Give the extent of all Plasmodium falciparum-infected red blood cells.
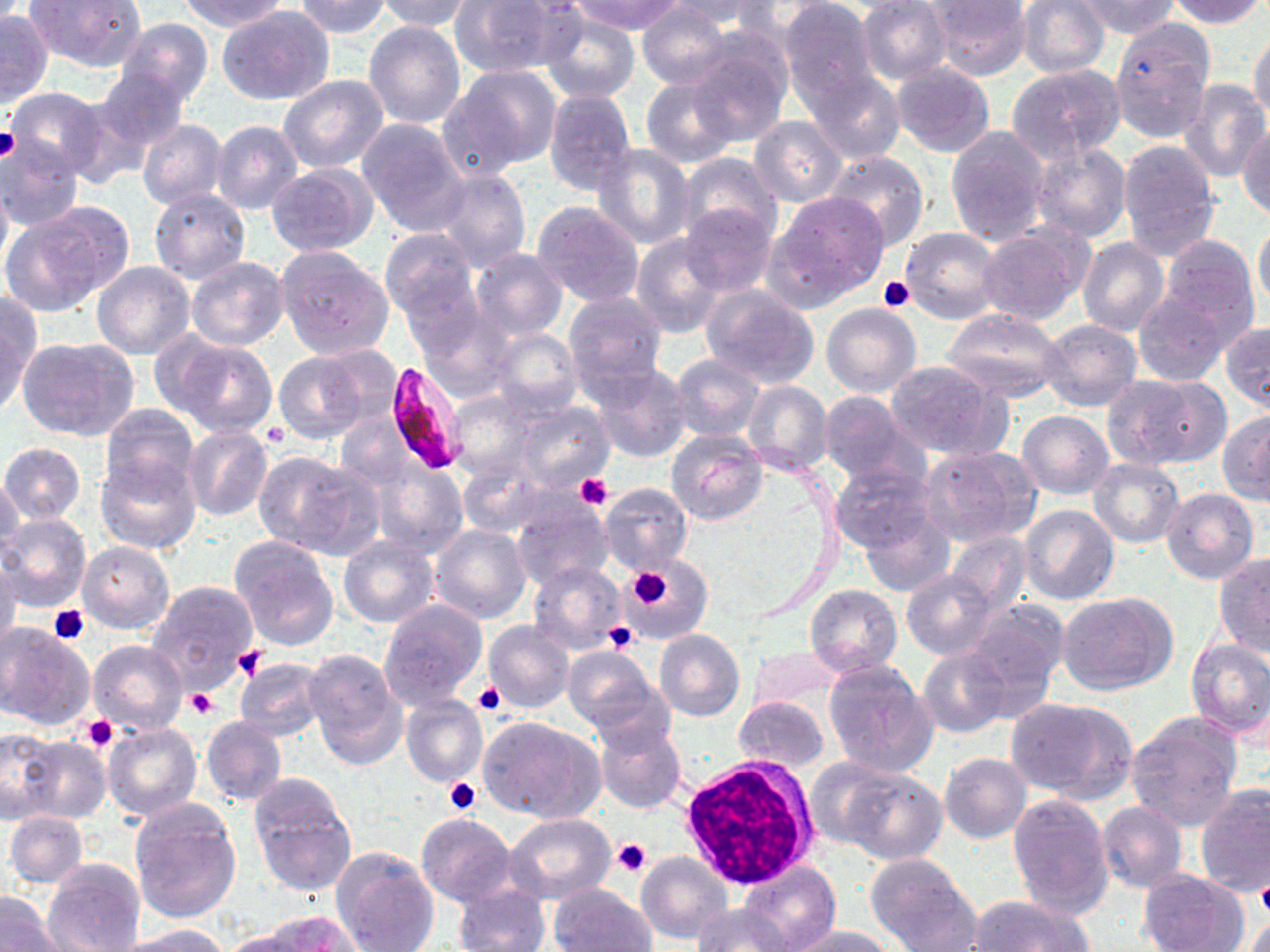

Approximate bounding boxes as [x1, y1, x2, y2] in pixels.
Plasmodium falciparum-infected red blood cells: [383, 361, 466, 475].

Summary:
  - White blood cell locations: [677, 756, 819, 887]
  - Platelet locations: [0, 128, 20, 163], [878, 276, 915, 313], [576, 474, 611, 510], [625, 566, 674, 609], [48, 604, 89, 645], [604, 621, 640, 654], [233, 645, 266, 679], [474, 681, 504, 715], [186, 689, 219, 719], [82, 714, 119, 753], [444, 777, 482, 815], [612, 838, 651, 877], [1255, 881, 1270, 917]
  - Uninfected red blood cell locations: [28, 0, 147, 72], [173, 0, 291, 32], [295, 0, 391, 38], [375, 0, 476, 33], [452, 0, 574, 81], [573, 0, 684, 36], [667, 0, 779, 30], [857, 0, 953, 86], [1073, 0, 1182, 39], [1163, 0, 1266, 27], [779, 1, 880, 107], [925, 1, 1031, 79], [1018, 1, 1111, 79], [636, 3, 730, 90], [217, 5, 334, 106], [538, 9, 640, 104], [0, 10, 52, 106], [115, 19, 215, 106], [363, 21, 466, 129], [1110, 24, 1215, 141], [1249, 26, 1270, 125], [683, 32, 792, 146], [891, 62, 995, 157], [1007, 63, 1125, 161], [444, 64, 563, 174], [94, 67, 189, 153], [804, 70, 905, 165], [279, 74, 389, 171], [640, 75, 741, 167], [1179, 79, 1269, 182], [5, 87, 109, 178], [1134, 87, 1258, 231], [543, 90, 636, 195], [748, 116, 848, 207], [211, 119, 304, 215], [357, 119, 470, 233], [136, 120, 228, 211], [1238, 124, 1270, 220], [944, 125, 1050, 244], [0, 138, 87, 232], [1116, 139, 1220, 256], [1029, 142, 1131, 242], [593, 144, 694, 249], [823, 150, 928, 249], [676, 153, 782, 247], [267, 162, 379, 258], [434, 166, 531, 271], [0, 174, 12, 285], [148, 186, 251, 282], [769, 192, 889, 305], [532, 201, 645, 306], [677, 201, 780, 298], [8, 203, 131, 312], [1254, 218, 1270, 315], [978, 225, 1090, 324], [900, 227, 1003, 324], [381, 228, 479, 322], [631, 233, 729, 337], [1156, 236, 1261, 341], [1077, 238, 1169, 337], [276, 247, 395, 358], [471, 247, 567, 338], [187, 256, 289, 350], [92, 262, 196, 359], [701, 285, 820, 388], [1131, 291, 1231, 384], [561, 292, 667, 391], [1, 294, 36, 412], [416, 299, 514, 397], [821, 303, 920, 396], [943, 306, 1065, 401], [1037, 319, 1141, 412], [1221, 322, 1269, 412], [488, 328, 582, 417], [19, 336, 139, 442], [168, 337, 279, 438], [275, 353, 372, 443], [672, 354, 763, 441], [884, 361, 1007, 459], [590, 364, 693, 463], [1107, 374, 1224, 469], [741, 381, 833, 477], [449, 390, 540, 479], [818, 391, 922, 485], [514, 401, 615, 493], [99, 403, 199, 500], [1018, 410, 1114, 499], [1218, 411, 1270, 506], [183, 426, 274, 521], [666, 429, 766, 524], [1, 442, 86, 524], [918, 444, 1040, 549], [252, 450, 376, 556], [96, 454, 201, 556], [458, 455, 549, 536], [369, 458, 467, 557], [1089, 458, 1184, 546], [830, 463, 936, 554], [1, 476, 25, 567], [600, 482, 692, 575], [1162, 488, 1259, 584], [510, 493, 613, 592], [1020, 504, 1119, 605], [859, 507, 956, 598], [0, 512, 91, 613], [429, 525, 531, 625], [946, 532, 1030, 614], [338, 535, 437, 627], [228, 536, 340, 650], [77, 541, 175, 634], [1214, 554, 1270, 653], [624, 557, 710, 641], [0, 558, 21, 656], [529, 562, 625, 654], [901, 570, 998, 660], [147, 580, 260, 693], [804, 584, 902, 677], [1056, 592, 1177, 696], [379, 598, 487, 708], [964, 600, 1067, 709], [0, 619, 95, 729], [482, 621, 574, 712], [655, 629, 744, 722], [1185, 637, 1270, 738], [88, 640, 187, 734], [562, 646, 667, 738], [748, 647, 843, 710], [304, 648, 408, 768], [917, 648, 1010, 738], [235, 658, 328, 742], [822, 661, 937, 778], [400, 695, 488, 788], [734, 696, 828, 772], [1005, 697, 1134, 802], [1126, 711, 1243, 829], [201, 716, 287, 804], [479, 716, 603, 824], [594, 717, 686, 814], [103, 721, 203, 821], [0, 728, 60, 821], [14, 736, 112, 825], [939, 752, 1032, 843], [803, 756, 911, 853], [837, 767, 946, 865], [250, 778, 357, 896], [1195, 786, 1269, 896], [1008, 793, 1114, 917], [129, 800, 240, 924], [1096, 800, 1187, 892], [5, 811, 88, 888], [505, 813, 615, 903], [415, 814, 516, 908], [331, 847, 440, 951], [638, 851, 732, 944], [865, 853, 978, 951], [42, 859, 146, 952], [736, 860, 843, 952], [1139, 870, 1248, 952], [548, 883, 655, 952], [452, 884, 549, 951], [0, 892, 64, 952], [970, 896, 1093, 952], [693, 902, 790, 951], [1240, 910, 1270, 951], [260, 913, 360, 952], [122, 923, 237, 952], [785, 926, 894, 952], [216, 929, 313, 952]
  - Slide-level diagnosis: Plasmodium falciparum
  - Preparation: thin blood smear
  - Modality: optical microscopy
  - Field of view: single
  - Image size: 1270×952 pixels
  - Magnification: 1000x
  - Stain: May-Grünwald-Giemsa